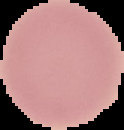
Summary:
  - Malaria status: uninfected
  - Image size: 124×130 pixels
  - Preparation: thin blood film
  - Image type: cell region segmented out of the field of view; surrounding area masked to black